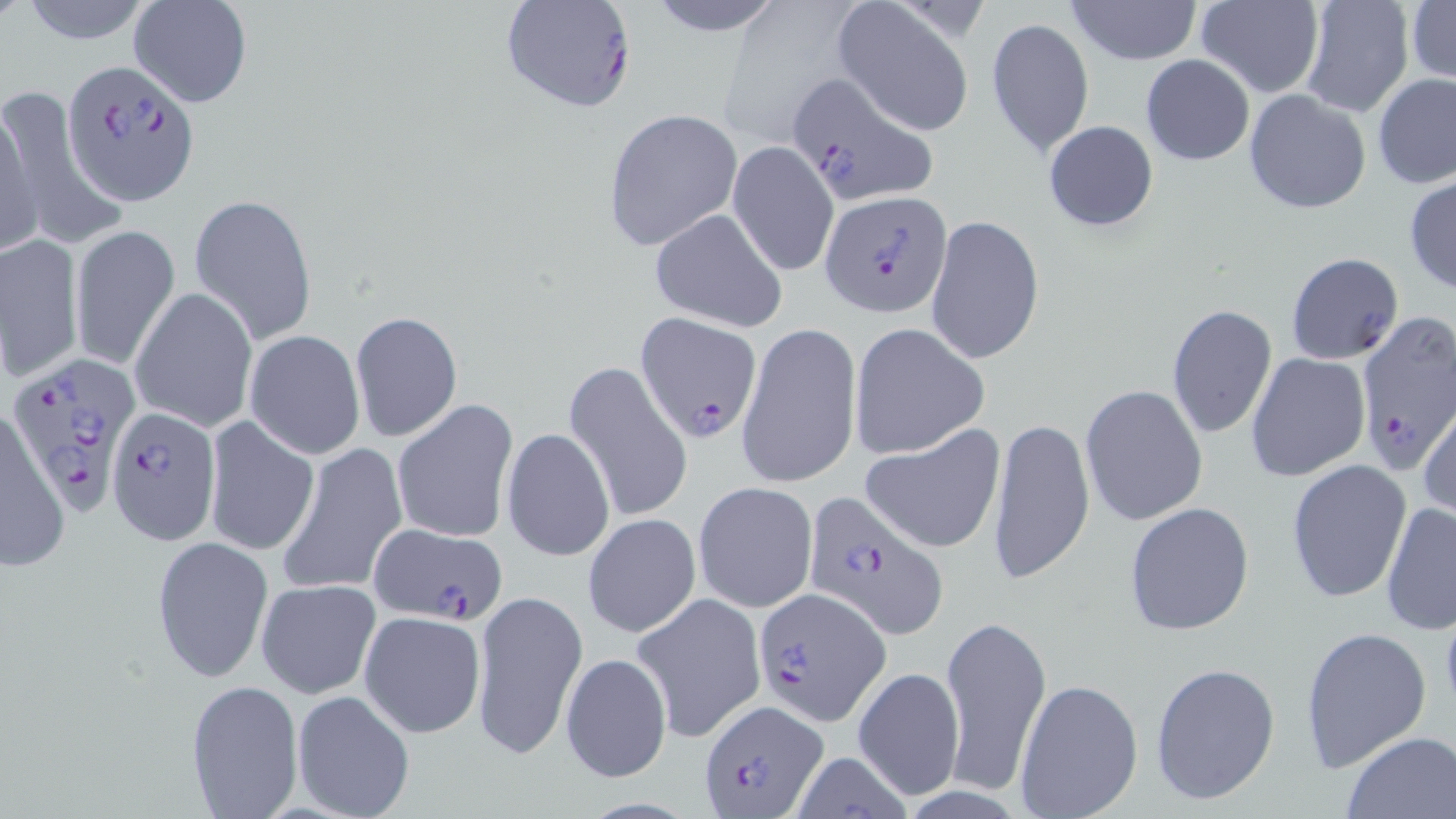 Approximate bounding boxes as named x1/y1/x2/y2 corners in pixels. Plasmodium falciparum-infected red blood cell locations: (x1=499, y1=0, x2=638, y2=115), (x1=65, y1=59, x2=198, y2=206), (x1=786, y1=73, x2=939, y2=206), (x1=820, y1=191, x2=951, y2=315), (x1=635, y1=312, x2=762, y2=443), (x1=1354, y1=313, x2=1456, y2=474), (x1=15, y1=354, x2=141, y2=513), (x1=104, y1=407, x2=219, y2=544), (x1=803, y1=489, x2=949, y2=639), (x1=369, y1=522, x2=510, y2=623), (x1=753, y1=588, x2=890, y2=723), (x1=697, y1=698, x2=828, y2=816). Uninfected red blood cell locations: (x1=16, y1=0, x2=161, y2=46), (x1=128, y1=0, x2=252, y2=108), (x1=639, y1=0, x2=790, y2=36), (x1=1064, y1=0, x2=1204, y2=66), (x1=1196, y1=0, x2=1324, y2=98), (x1=1298, y1=0, x2=1415, y2=119), (x1=1406, y1=1, x2=1455, y2=87), (x1=832, y1=2, x2=976, y2=136), (x1=987, y1=16, x2=1094, y2=157), (x1=1139, y1=54, x2=1255, y2=166), (x1=1372, y1=73, x2=1456, y2=189), (x1=2, y1=86, x2=118, y2=246), (x1=1243, y1=88, x2=1372, y2=214), (x1=0, y1=96, x2=43, y2=256), (x1=602, y1=108, x2=743, y2=255), (x1=1043, y1=120, x2=1159, y2=233), (x1=727, y1=141, x2=839, y2=277), (x1=1404, y1=174, x2=1456, y2=295), (x1=189, y1=194, x2=317, y2=347), (x1=649, y1=209, x2=789, y2=332), (x1=926, y1=214, x2=1045, y2=368), (x1=71, y1=224, x2=179, y2=368), (x1=0, y1=232, x2=85, y2=386), (x1=1286, y1=253, x2=1402, y2=364), (x1=130, y1=287, x2=255, y2=433), (x1=1167, y1=304, x2=1278, y2=439), (x1=350, y1=311, x2=463, y2=443), (x1=735, y1=319, x2=860, y2=491), (x1=847, y1=323, x2=988, y2=460), (x1=243, y1=329, x2=365, y2=459), (x1=1245, y1=352, x2=1370, y2=483), (x1=562, y1=361, x2=693, y2=524), (x1=1079, y1=384, x2=1207, y2=526), (x1=394, y1=399, x2=520, y2=546), (x1=1418, y1=401, x2=1456, y2=520), (x1=0, y1=408, x2=69, y2=573), (x1=988, y1=417, x2=1094, y2=586), (x1=203, y1=419, x2=317, y2=557), (x1=862, y1=423, x2=1008, y2=554), (x1=501, y1=428, x2=615, y2=562), (x1=277, y1=441, x2=408, y2=598), (x1=1285, y1=459, x2=1412, y2=603), (x1=693, y1=482, x2=818, y2=612), (x1=1380, y1=499, x2=1456, y2=636), (x1=1123, y1=502, x2=1255, y2=635), (x1=583, y1=514, x2=701, y2=639), (x1=152, y1=535, x2=273, y2=685), (x1=255, y1=579, x2=381, y2=700), (x1=472, y1=590, x2=586, y2=761), (x1=631, y1=592, x2=766, y2=742), (x1=359, y1=610, x2=486, y2=739), (x1=940, y1=610, x2=1052, y2=797), (x1=1299, y1=626, x2=1432, y2=772), (x1=560, y1=651, x2=670, y2=783), (x1=1150, y1=661, x2=1280, y2=805), (x1=854, y1=666, x2=964, y2=800), (x1=1015, y1=679, x2=1144, y2=816), (x1=185, y1=680, x2=304, y2=815), (x1=292, y1=690, x2=416, y2=819), (x1=1342, y1=731, x2=1456, y2=817), (x1=788, y1=751, x2=913, y2=819). Slide-level diagnosis: Plasmodium falciparum. Thin blood film. May-Grünwald-Giemsa stain. Light microscopy. Single field of view. Captured at 1000x magnification. Image is 1456×819 pixels.